Name the blood parasite species.
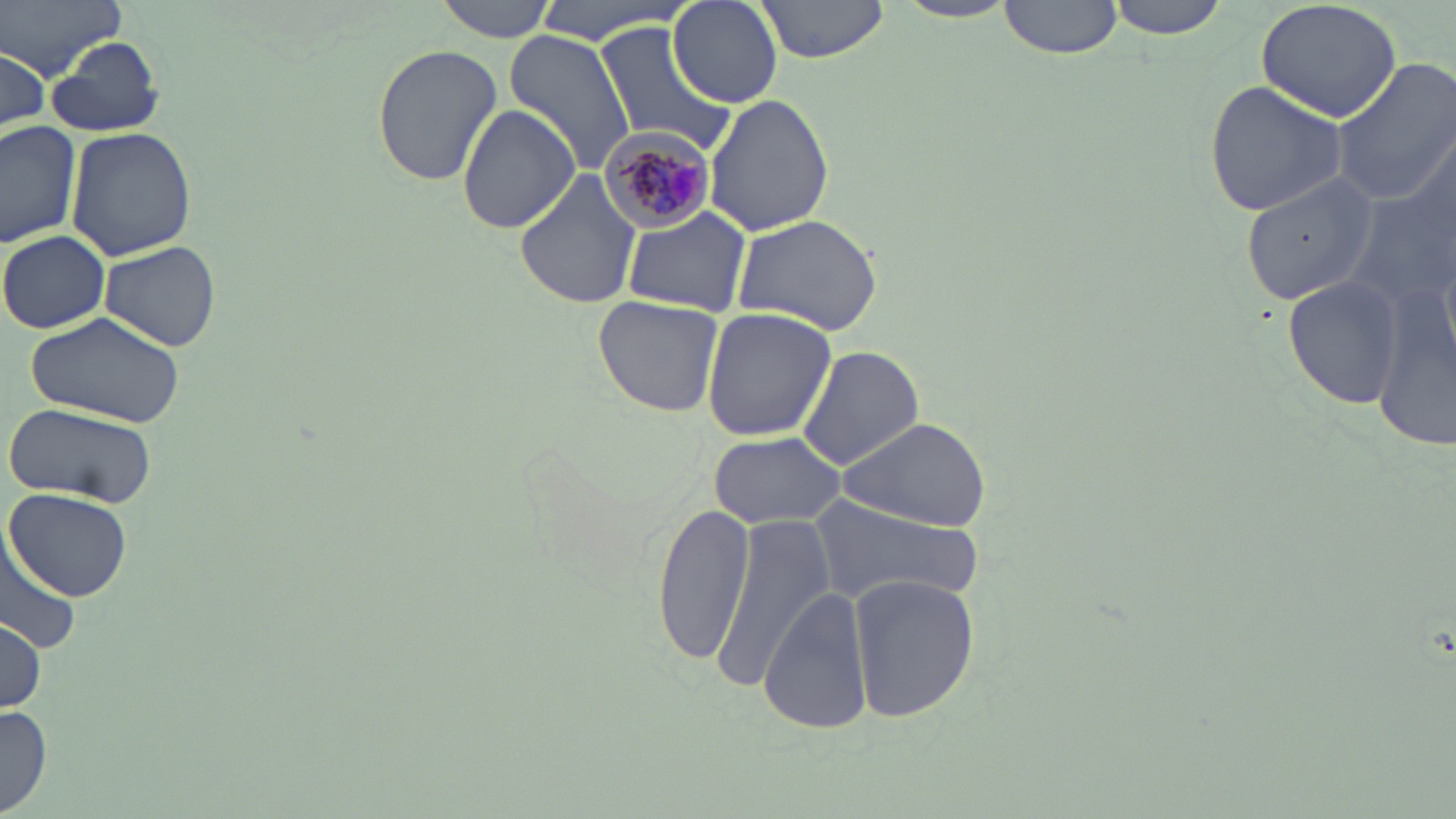
Plasmodium malariae.

Approximate bounding boxes as (x1, y1, x2, y2) in pixels. Plasmodium malariae-infected red blood cell locations: (597, 122, 717, 233). Uninfected red blood cell locations: (2, 0, 126, 75), (431, 0, 558, 42), (533, 0, 694, 45), (668, 0, 783, 109), (753, 0, 890, 63), (998, 0, 1126, 60), (1101, 0, 1237, 38), (1256, 0, 1401, 122), (892, 2, 1021, 25), (593, 23, 737, 153), (504, 28, 636, 176), (45, 37, 165, 138), (370, 44, 502, 184), (0, 45, 50, 134), (1328, 57, 1456, 209), (1204, 80, 1348, 217), (704, 93, 835, 236), (457, 103, 580, 234), (0, 119, 83, 248), (67, 127, 197, 259), (1353, 159, 1455, 445), (513, 169, 642, 311), (1239, 172, 1379, 305), (622, 208, 750, 316), (732, 211, 885, 337), (1, 230, 110, 334), (99, 242, 222, 350), (1283, 276, 1404, 408), (592, 296, 724, 418), (701, 306, 837, 440), (24, 310, 187, 429), (796, 345, 924, 471), (8, 404, 159, 506), (836, 415, 991, 530), (707, 432, 846, 530), (6, 487, 133, 601), (808, 496, 982, 609), (652, 502, 758, 669), (713, 518, 836, 688), (0, 533, 81, 659), (846, 572, 981, 724), (760, 585, 874, 736), (1, 614, 45, 713), (0, 705, 53, 815). Image is 1456×819 pixels. Optical microscopy. Single field of view. May-Grünwald-Giemsa-stained preparation. Captured at 1000x magnification. Thin blood film.